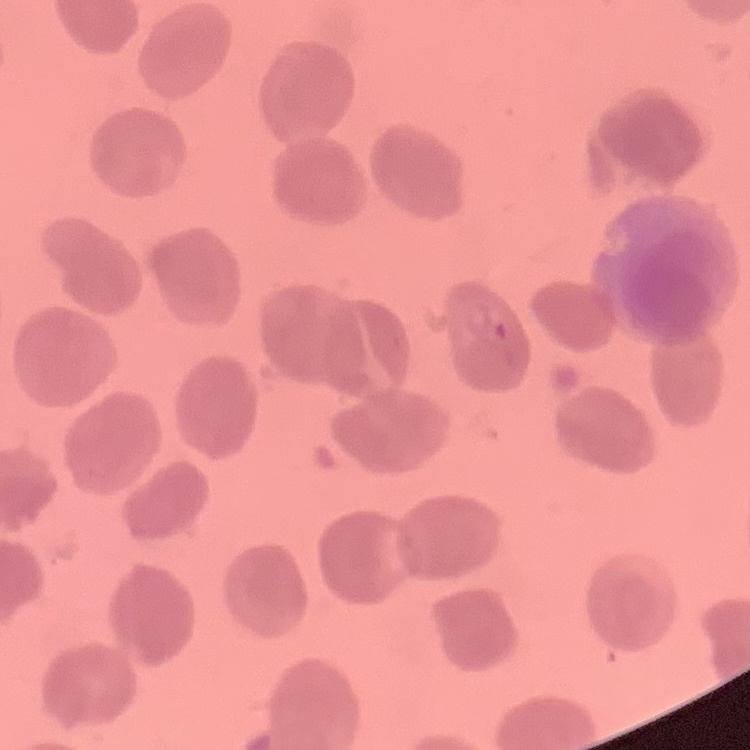

erythrocyte_morphology: no rouleaux formation
stain: Field's or Giemsa
preparation: thin blood film
image_type: one tile cut from a larger photomicrograph